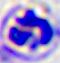

Captured at 400x magnification. Micrograph. A leukocyte is shown.